Name the cell type shown.
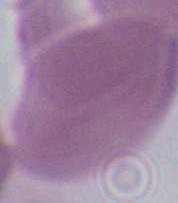

An erythrocyte.

Summary:
  - Magnification: 1000x
  - Modality: photomicrograph